Give the position of every Plasmodium parasite.
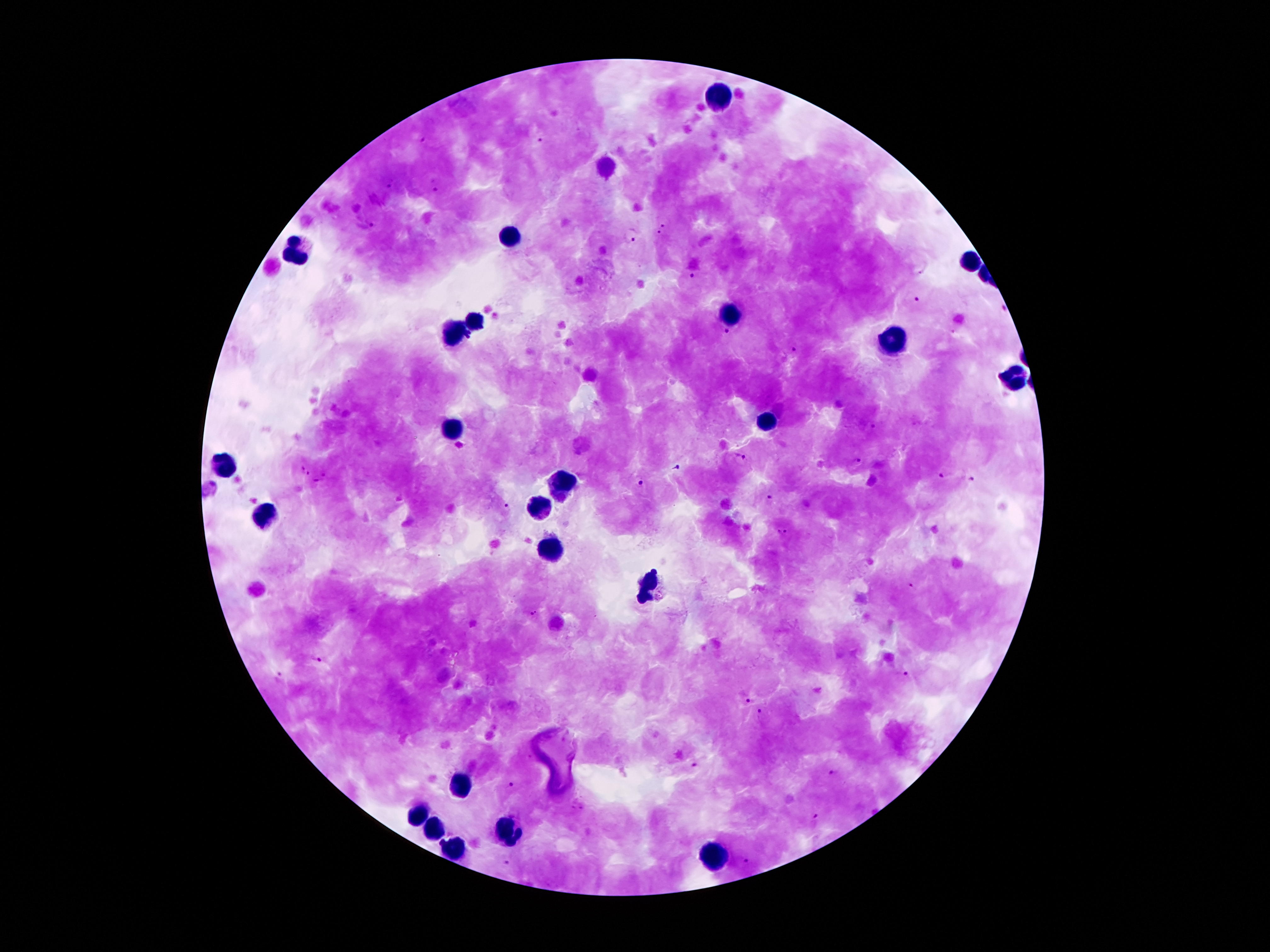

Approximate centers as {x, y} in pixels.
Plasmodium parasites: {421, 138}, {541, 138}, {387, 184}, {435, 187}, {666, 219}, {372, 224}, {659, 236}, {631, 238}, {691, 277}, {918, 300}, {1002, 307}, {726, 333}, {791, 349}, {871, 426}, {739, 459}, {857, 461}, {675, 468}, {305, 469}, {945, 476}, {972, 481}, {642, 483}, {770, 497}, {505, 506}, {784, 532}, {913, 585}, {535, 614}, {316, 659}, {904, 674}, {278, 675}, {746, 698}, {760, 714}, {694, 764}, {833, 773}, {510, 785}, {814, 818}, {508, 861}, {748, 862}.

Leukocyte locations: {722, 96}, {513, 232}, {296, 250}, {966, 262}, {730, 314}, {474, 322}, {456, 332}, {898, 344}, {1015, 376}, {769, 421}, {454, 429}, {224, 465}, {560, 487}, {538, 508}, {265, 517}, {552, 549}, {650, 584}, {458, 785}, {415, 814}, {433, 827}, {509, 832}, {453, 849}, {716, 854}. Photographed through the microscope eyepiece with a smartphone camera. Image is 1270×952 pixels. Patient malaria status: infected with Plasmodium falciparum. 100x magnification. Thick blood film. Giemsa-stained preparation. One field from this slide.